Assess this cell for malaria.
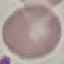
Uninfected.

Cell patch, automatically extracted from a larger field of view and resized to 64 × 64 pixels. Giemsa stain. Photographed with a smartphone camera at the microscope eyepiece. Thin blood film.